Classify this cell by malaria status.
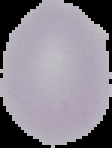
It is uninfected.

Summary:
  - Image size: 112×148 pixels
  - Preparation: thin blood film
  - Image type: segmented cell region with the area outside set to black